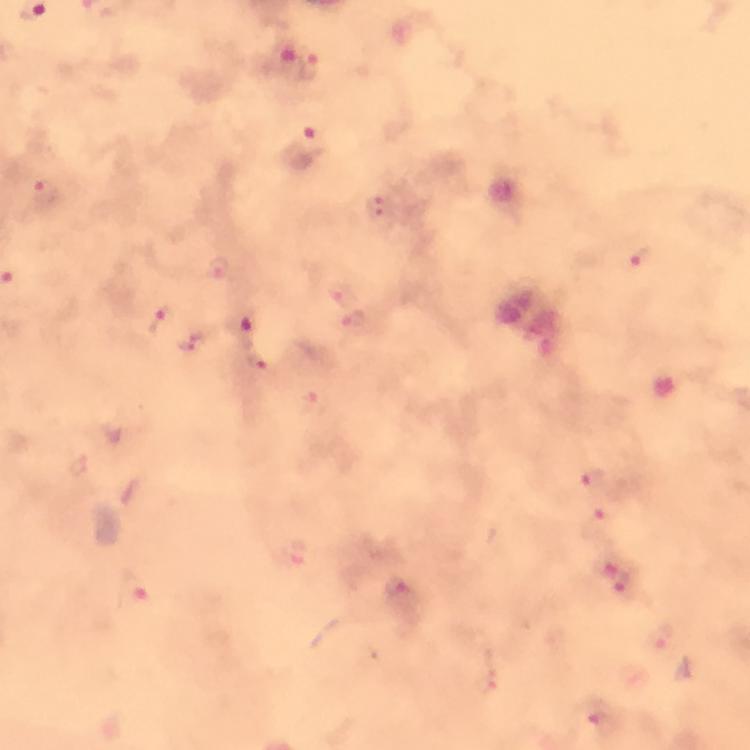 Approximate object centers, in pixels from the top-left corner. Malaria parasite locations: (x=308, y=69), (x=312, y=138), (x=46, y=193), (x=379, y=210), (x=642, y=259), (x=219, y=271), (x=336, y=293), (x=160, y=320), (x=353, y=321), (x=242, y=323), (x=261, y=362), (x=591, y=480), (x=599, y=524), (x=299, y=556), (x=619, y=577), (x=134, y=587), (x=401, y=594), (x=596, y=716). Immersion oil was used. Giemsa stain. Image is 750×750 pixels. Cropped region of a single field of view. Photographed with a smartphone mounted on the microscope. From a malaria diagnostic workup. At 100x magnification. Thick blood smear.